Assess the morphology of the erythrocytes.
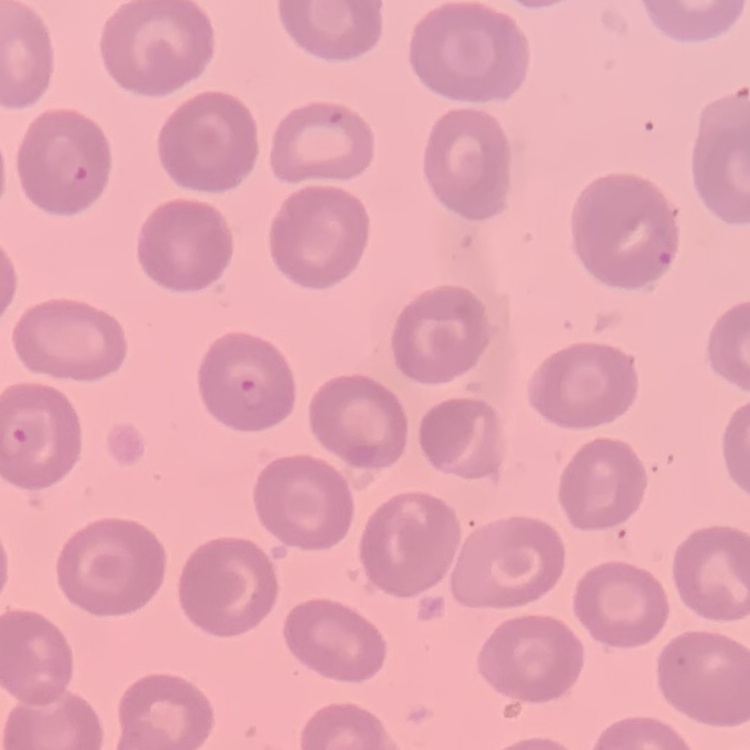
No rouleaux formation.

preparation = thin blood smear
stain = Field's or Giemsa
image type = one tile cut from a larger photomicrograph